Name the parasite shown.
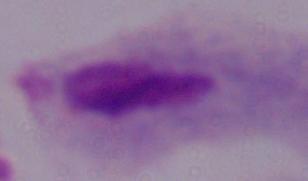

A trichomonad.

Micrograph. 1000x magnification.